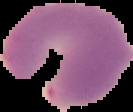
{
  "image_type": "cell region segmented out of the field of view; surrounding area masked to black",
  "image_size": "133×112 pixels",
  "preparation": "thin blood film",
  "malaria_status": "parasitized"
}